Identify the parasite.
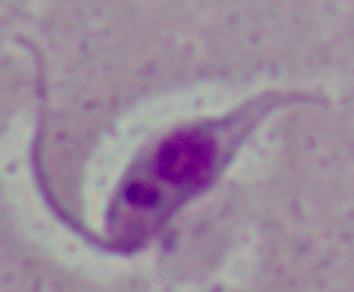
This is Leishmania.

Micrograph. Captured at 1000x magnification.